Outline platelets.
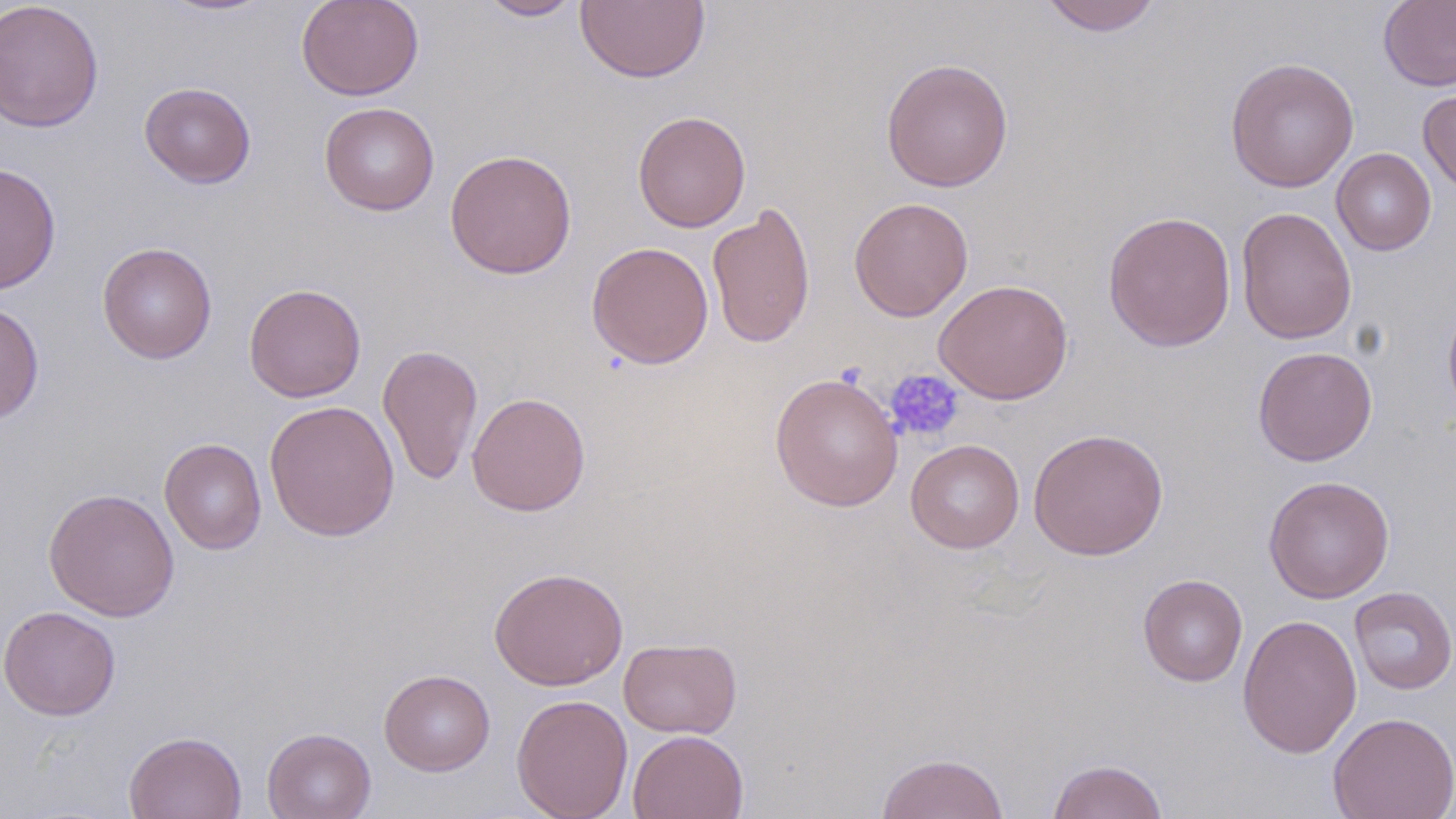

Approximate bounding boxes as (x1,y1)-(x2,y2) corner pairs in pixels.
Platelets: (885,369)-(965,443).

Uninfected red blood cell locations: (159,0)-(275,17), (296,0)-(424,101), (477,0)-(586,21), (575,0)-(710,84), (1038,0)-(1163,36), (1378,0)-(1456,92), (0,1)-(105,134), (880,57)-(1014,192), (1224,57)-(1359,193), (139,82)-(256,188), (1418,84)-(1456,195), (319,102)-(439,216), (632,111)-(751,233), (1331,148)-(1436,255), (445,149)-(577,279), (0,162)-(61,295), (848,197)-(974,322), (706,202)-(816,349), (1235,206)-(1357,345), (1102,210)-(1237,352), (586,241)-(714,369), (97,242)-(217,363), (934,279)-(1073,404), (243,283)-(366,403), (1442,296)-(1456,427), (0,300)-(44,424), (377,343)-(483,486), (1252,346)-(1378,466), (769,372)-(904,512), (467,392)-(591,516), (263,399)-(400,541), (1028,427)-(1168,560), (160,438)-(267,555), (905,438)-(1024,553), (1263,475)-(1394,603), (43,487)-(180,621), (488,566)-(628,691), (1138,573)-(1248,686), (1349,586)-(1456,695), (1,606)-(121,720), (1237,613)-(1362,759), (618,637)-(742,738), (379,669)-(495,776), (511,694)-(633,819), (1328,711)-(1456,818), (262,727)-(376,819), (627,729)-(748,819), (124,730)-(247,819), (876,752)-(1010,819), (1047,759)-(1168,819). Slide-level diagnosis: negative for blood parasites. Optical microscopy. One field of a larger specimen. Thin blood smear. May-Grünwald-Giemsa stain. Image is 1456×819 pixels. 1000x magnification.